Locate and identify every blood parasite.
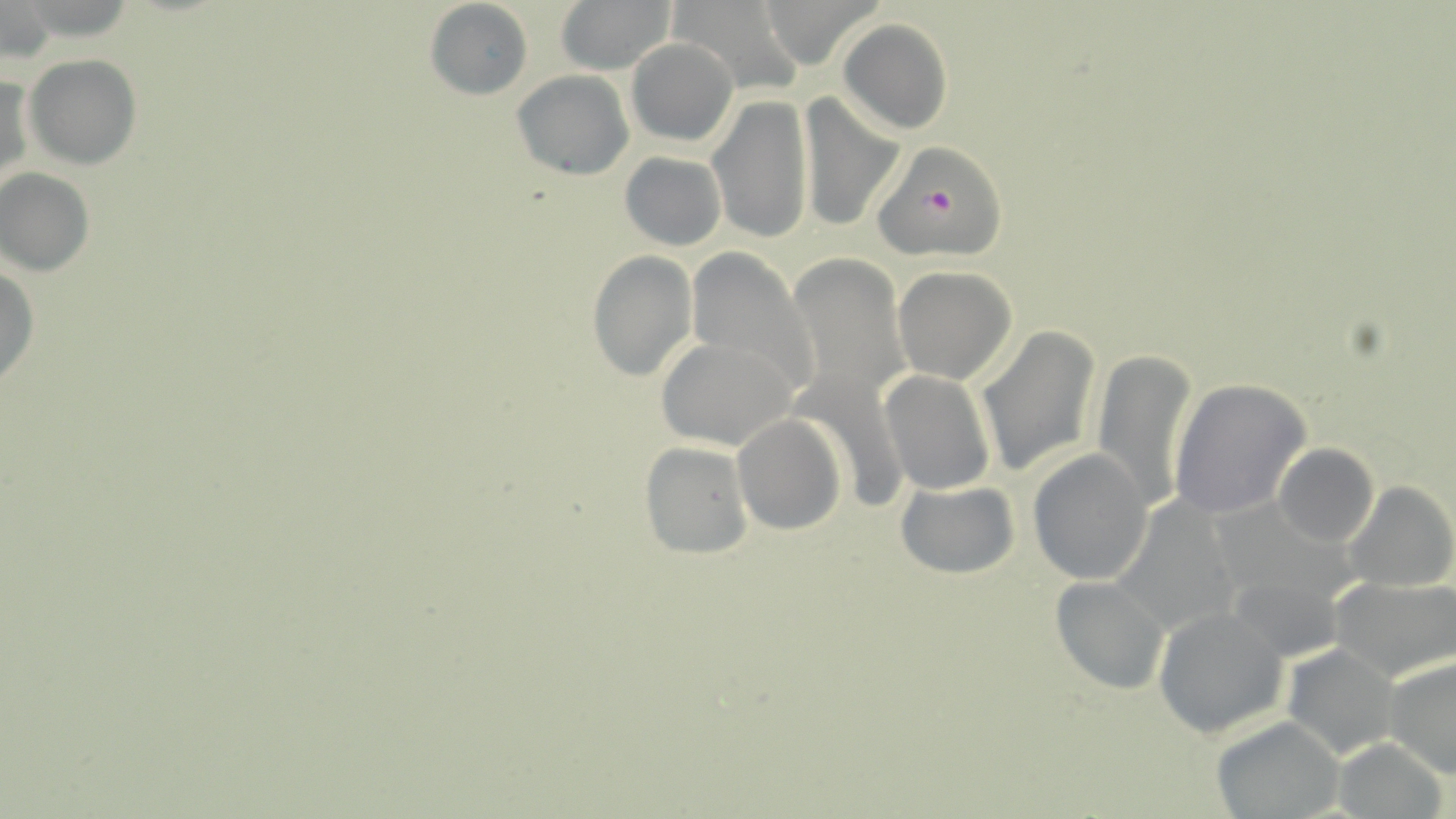

Approximate bounding boxes as (x1, y1, x2, y2) in pixels.
Plasmodium falciparum-infected red blood cells: (872, 146, 1012, 261).
No Plasmodium ovale, Plasmodium malariae, Plasmodium vivax, Babesia divergens, or Trypanosoma brucei observed.

Uninfected red blood cell locations: (553, 0, 677, 74), (669, 0, 805, 93), (760, 0, 883, 70), (425, 1, 534, 100), (0, 2, 52, 63), (838, 19, 953, 136), (625, 38, 737, 147), (25, 54, 141, 168), (511, 69, 635, 180), (1, 71, 34, 193), (800, 90, 902, 232), (707, 94, 816, 245), (618, 151, 727, 251), (0, 169, 95, 275), (687, 249, 818, 396), (586, 250, 698, 381), (789, 254, 909, 403), (0, 265, 39, 390), (891, 265, 1018, 385), (980, 325, 1101, 475), (656, 337, 798, 451), (1091, 347, 1197, 514), (791, 365, 910, 513), (879, 369, 997, 496), (1169, 378, 1311, 520), (733, 414, 847, 535), (638, 440, 754, 560), (1272, 443, 1378, 548), (1026, 448, 1153, 585), (895, 480, 1019, 580), (1343, 481, 1456, 593), (1111, 495, 1242, 634), (1220, 544, 1358, 661), (1050, 576, 1172, 694), (1330, 577, 1456, 683), (1153, 607, 1290, 739), (1282, 644, 1398, 760), (1385, 653, 1456, 779), (1211, 716, 1346, 819), (1331, 738, 1449, 818). Slide-level diagnosis: Plasmodium falciparum. Image is 1456×819 pixels. May-Grünwald-Giemsa-stained preparation. Captured at 1000x magnification. Optical microscopy. Thin blood smear. One field of a larger specimen.